Name the parasite shown.
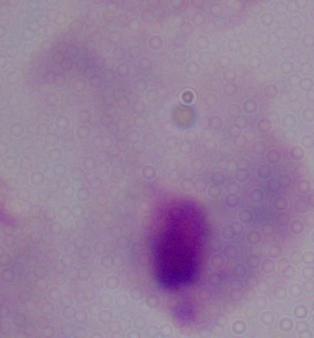
A trichomonad.

Summary:
  - Magnification: 1000x
  - Modality: micrograph